Identify the cell.
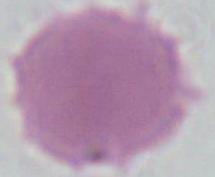
An erythrocyte.

Micrograph. Captured at 1000x magnification.